Report the malaria status of this cell.
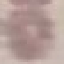
Uninfected.

Summary:
  - Stain: Giemsa
  - Image type: automatically extracted cell patch, resized to 64 × 64 pixels
  - Capture: smartphone through the microscope eyepiece
  - Preparation: thin blood film